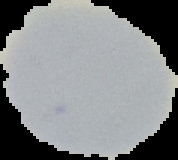

Result: negative for Plasmodium parasites. The area outside the segmented cell region is set to black. Image is 178×160 pixels. From a thin blood smear.